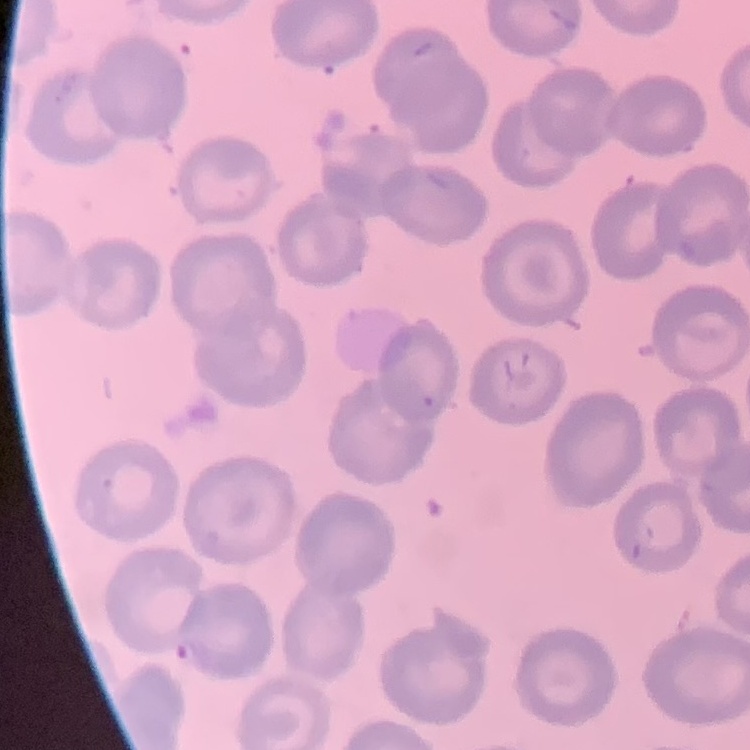

{
  "erythrocyte_morphology": "no rouleaux formation",
  "image_type": "square crop of a larger photomicrograph",
  "stain": "Field's or Giemsa",
  "preparation": "thin blood film"
}